State which parasite is depicted.
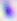

Toxoplasma gondii.

modality = micrograph
magnification = 400x